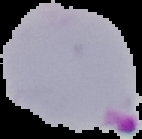

Summary:
  - Image size: 142×139 pixels
  - Malaria status: parasitized
  - Image type: segmented cell region with the area outside set to black
  - Preparation: thin blood film